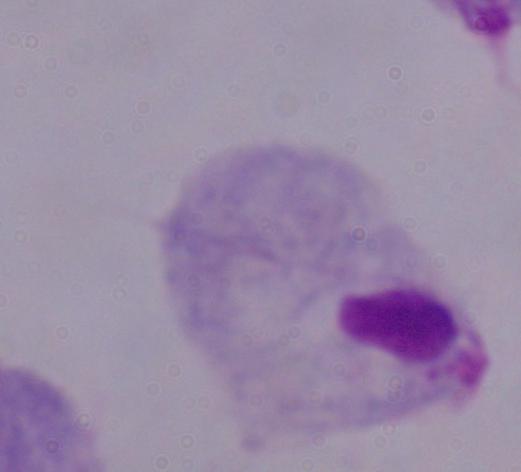
magnification = 1000x
identification = trichomonad
modality = micrograph